Assess this cell for malaria.
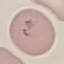
Parasitized.

Summary:
  - Capture: smartphone through the microscope eyepiece
  - Preparation: thin blood film
  - Stain: Giemsa
  - Image type: cell patch, automatically extracted from a larger field of view and resized to 64 × 64 pixels